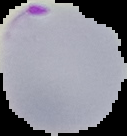

image type = segmented cell region on a black background
result = Plasmodium parasites identified
image size = 127×136 pixels
preparation = thin blood smear